Assess this cell for malaria.
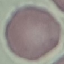

Uninfected.

Photographed with a smartphone camera at the microscope eyepiece. Giemsa stain. Automatically extracted cell patch, resized to 64 × 64 pixels. Thin blood smear.